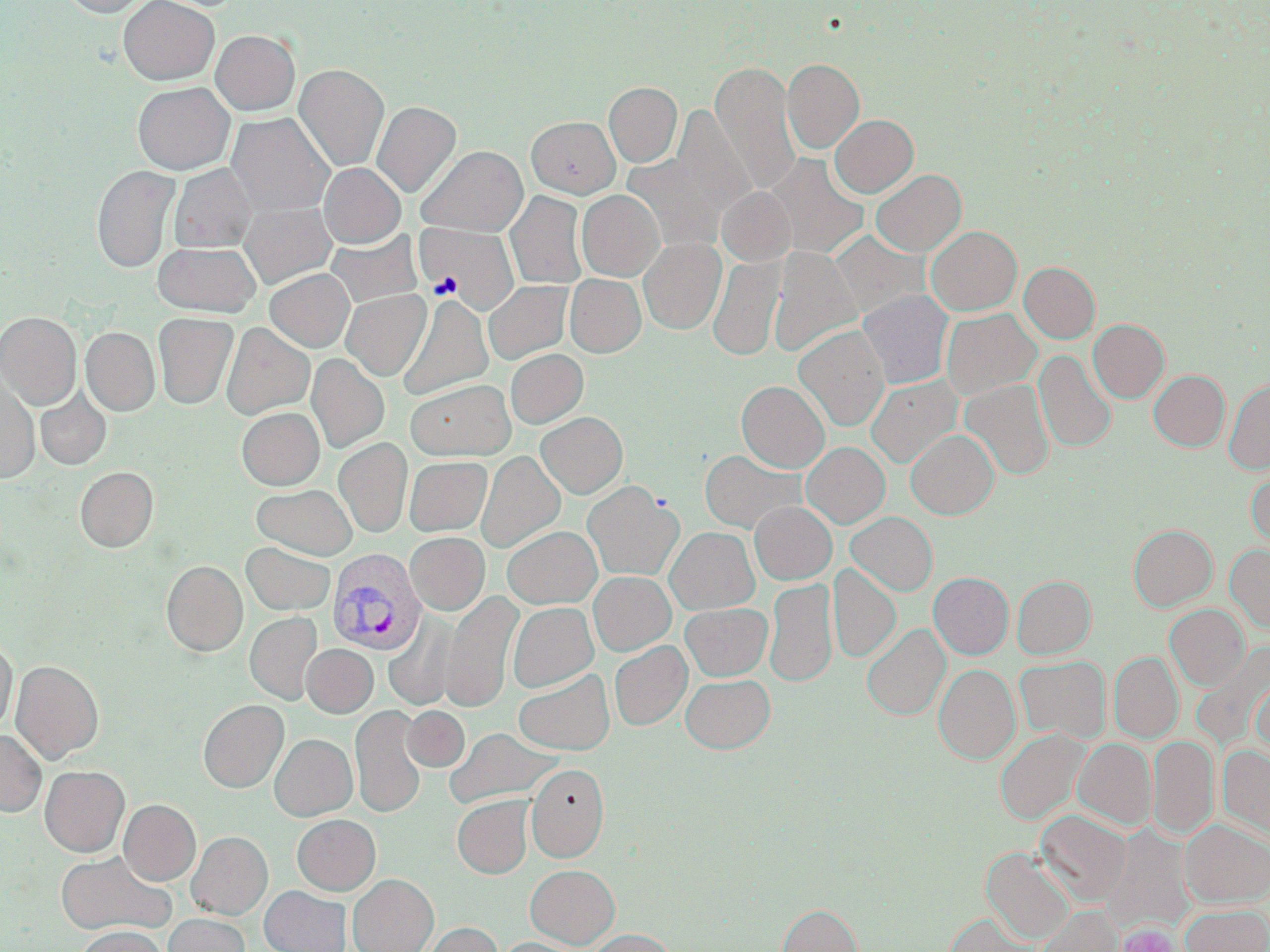
Summary:
  - Coordinate format: approximate bounding boxes as named x1/y1/x2/y2 corners in pixels
  - Uninfected red blood cell locations: (x1=61, y1=0, x2=151, y2=17), (x1=119, y1=0, x2=219, y2=84), (x1=211, y1=30, x2=300, y2=115), (x1=782, y1=58, x2=864, y2=154), (x1=711, y1=63, x2=800, y2=194), (x1=294, y1=64, x2=389, y2=171), (x1=133, y1=82, x2=234, y2=174), (x1=604, y1=82, x2=682, y2=167), (x1=372, y1=101, x2=461, y2=198), (x1=657, y1=104, x2=756, y2=232), (x1=227, y1=113, x2=334, y2=216), (x1=830, y1=114, x2=918, y2=197), (x1=526, y1=116, x2=620, y2=198), (x1=417, y1=146, x2=527, y2=236), (x1=764, y1=154, x2=869, y2=259), (x1=319, y1=163, x2=405, y2=247), (x1=170, y1=164, x2=257, y2=252), (x1=92, y1=165, x2=180, y2=272), (x1=871, y1=169, x2=966, y2=256), (x1=717, y1=187, x2=795, y2=266), (x1=577, y1=190, x2=664, y2=281), (x1=506, y1=191, x2=587, y2=289), (x1=239, y1=202, x2=336, y2=288), (x1=421, y1=224, x2=519, y2=313), (x1=926, y1=226, x2=1021, y2=314), (x1=830, y1=230, x2=929, y2=318), (x1=326, y1=232, x2=422, y2=309), (x1=639, y1=238, x2=725, y2=334), (x1=153, y1=241, x2=260, y2=316), (x1=769, y1=248, x2=860, y2=356), (x1=708, y1=255, x2=784, y2=361), (x1=1019, y1=262, x2=1100, y2=343), (x1=265, y1=268, x2=354, y2=352), (x1=565, y1=274, x2=645, y2=357), (x1=484, y1=281, x2=572, y2=364), (x1=341, y1=289, x2=430, y2=381), (x1=858, y1=290, x2=954, y2=388), (x1=398, y1=294, x2=493, y2=400), (x1=941, y1=308, x2=1041, y2=399), (x1=0, y1=312, x2=81, y2=409), (x1=153, y1=313, x2=238, y2=409), (x1=1088, y1=319, x2=1168, y2=403), (x1=222, y1=323, x2=314, y2=419), (x1=793, y1=325, x2=889, y2=431), (x1=81, y1=327, x2=159, y2=416), (x1=505, y1=349, x2=588, y2=428), (x1=1035, y1=350, x2=1117, y2=452), (x1=307, y1=354, x2=389, y2=453), (x1=1149, y1=370, x2=1229, y2=451), (x1=866, y1=375, x2=962, y2=468), (x1=0, y1=377, x2=39, y2=483), (x1=405, y1=379, x2=514, y2=460), (x1=961, y1=379, x2=1054, y2=480), (x1=1224, y1=379, x2=1270, y2=474), (x1=736, y1=381, x2=829, y2=472), (x1=35, y1=389, x2=111, y2=470), (x1=237, y1=407, x2=324, y2=489), (x1=536, y1=412, x2=627, y2=498), (x1=906, y1=429, x2=998, y2=518), (x1=334, y1=438, x2=412, y2=537), (x1=802, y1=442, x2=890, y2=528), (x1=700, y1=450, x2=803, y2=532), (x1=477, y1=451, x2=565, y2=553), (x1=405, y1=456, x2=492, y2=536), (x1=75, y1=467, x2=158, y2=552), (x1=1246, y1=468, x2=1270, y2=549), (x1=583, y1=482, x2=683, y2=580), (x1=252, y1=484, x2=357, y2=559), (x1=750, y1=501, x2=836, y2=584), (x1=847, y1=512, x2=937, y2=595), (x1=1129, y1=525, x2=1217, y2=611), (x1=503, y1=526, x2=601, y2=608), (x1=665, y1=527, x2=759, y2=614), (x1=406, y1=533, x2=489, y2=615), (x1=242, y1=542, x2=334, y2=615), (x1=1225, y1=545, x2=1270, y2=633), (x1=162, y1=561, x2=247, y2=656), (x1=829, y1=564, x2=900, y2=662), (x1=589, y1=572, x2=675, y2=655), (x1=929, y1=572, x2=1013, y2=659), (x1=1012, y1=575, x2=1095, y2=658), (x1=765, y1=578, x2=837, y2=687), (x1=442, y1=590, x2=521, y2=712), (x1=508, y1=602, x2=598, y2=692), (x1=681, y1=603, x2=771, y2=681), (x1=1165, y1=604, x2=1249, y2=690), (x1=245, y1=613, x2=322, y2=704), (x1=384, y1=614, x2=460, y2=710), (x1=862, y1=624, x2=950, y2=720), (x1=0, y1=639, x2=16, y2=734), (x1=609, y1=642, x2=691, y2=730), (x1=302, y1=644, x2=377, y2=717), (x1=1109, y1=652, x2=1183, y2=742), (x1=1015, y1=656, x2=1110, y2=743), (x1=11, y1=661, x2=103, y2=763), (x1=934, y1=664, x2=1019, y2=764), (x1=514, y1=670, x2=614, y2=754), (x1=681, y1=674, x2=775, y2=753), (x1=1251, y1=678, x2=1270, y2=756), (x1=199, y1=699, x2=288, y2=792), (x1=351, y1=705, x2=426, y2=818), (x1=403, y1=706, x2=469, y2=771), (x1=445, y1=728, x2=559, y2=808), (x1=996, y1=729, x2=1087, y2=825), (x1=0, y1=730, x2=46, y2=816), (x1=270, y1=734, x2=357, y2=820), (x1=1148, y1=735, x2=1218, y2=839), (x1=1073, y1=738, x2=1156, y2=829), (x1=1218, y1=745, x2=1270, y2=837), (x1=526, y1=764, x2=609, y2=862), (x1=40, y1=766, x2=129, y2=856), (x1=452, y1=796, x2=533, y2=878), (x1=119, y1=799, x2=201, y2=885), (x1=1035, y1=811, x2=1130, y2=906), (x1=292, y1=814, x2=380, y2=895), (x1=1181, y1=820, x2=1270, y2=906), (x1=1104, y1=826, x2=1195, y2=933), (x1=187, y1=831, x2=272, y2=919), (x1=983, y1=848, x2=1074, y2=943), (x1=54, y1=851, x2=174, y2=936), (x1=526, y1=865, x2=619, y2=948), (x1=348, y1=874, x2=438, y2=952), (x1=259, y1=885, x2=351, y2=952), (x1=777, y1=903, x2=861, y2=952), (x1=1181, y1=905, x2=1270, y2=952), (x1=1037, y1=906, x2=1122, y2=952), (x1=163, y1=914, x2=250, y2=952), (x1=945, y1=914, x2=1036, y2=952), (x1=420, y1=922, x2=502, y2=952), (x1=75, y1=927, x2=166, y2=952), (x1=588, y1=929, x2=675, y2=952), (x1=499, y1=937, x2=583, y2=952)
  - Platelet locations: (x1=1117, y1=923, x2=1181, y2=952)
  - Plasmodium vivax-infected red blood cell locations: (x1=326, y1=548, x2=425, y2=654)
  - Slide-level diagnosis: Plasmodium vivax
  - Magnification: 1000x
  - Preparation: thin blood film
  - Image size: 1270×952 pixels
  - Field of view: one of a larger specimen
  - Modality: light microscopy
  - Stain: May-Grünwald-Giemsa